Identify the cell.
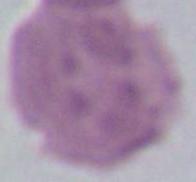

This is an erythrocyte.

{
  "modality": "micrograph",
  "magnification": "1000x"
}